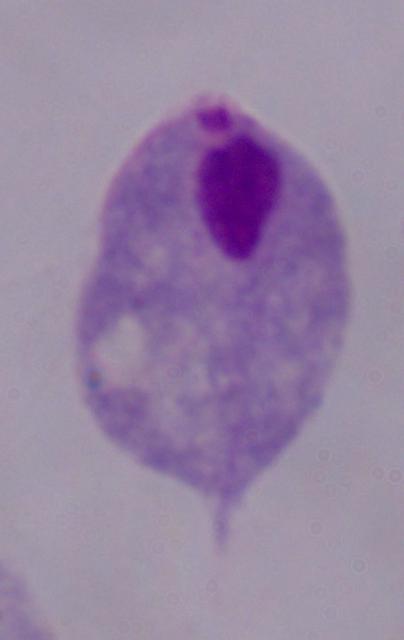
Micrograph. A trichomonad is shown. Captured at 1000x magnification.